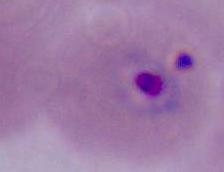

modality: micrograph
identification: Plasmodium
magnification: 400x or 1000x